State the preparation type.
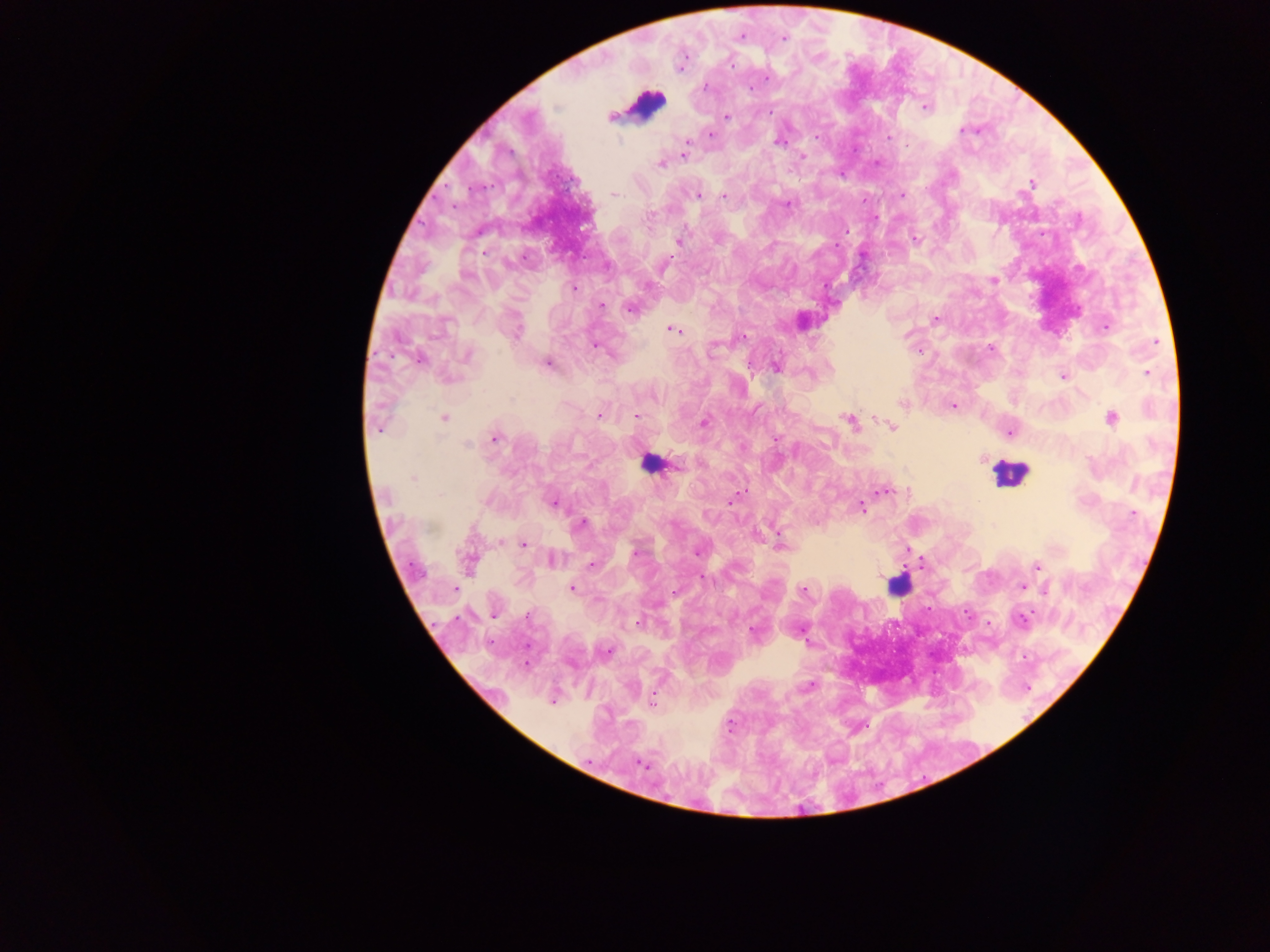

This is a thick smear.

plasmodium_parasite_locations: 'approximate centers as x y in pixels: 741 36; 783 38; 681 66; 705 87; 925 108; 727 117; 963 130; 711 134; 815 137; 889 137; 778 142; 687 143; 684 154; 802 157; 661 164; 1032 183; 614 194; 698 195; 902 195; 723 196; 788 205; 648 217; 916 238; 679 240; 993 280; 647 286; 573 288; 602 305; 631 309; 935 320; 1105 327; 674 330; 516 332; 743 337; 1155 342; 594 346; 990 348; 468 355; 418 359; 548 364; 776 367; 1147 373; 1063 376; 903 404; 954 405; 598 415; 636 416; 444 418; 1111 418; 849 420; 704 422; 892 427; 378 429; 1010 433; 495 438; 467 444; 413 478; 884 491; 737 496; 732 500; 554 503; 861 508; 1133 514; 581 524; 780 543; 523 544; 697 552; 635 553; 552 560; 468 562; 591 565; 1038 566; 703 578; 1021 587; 455 588; 573 588; 1046 589; 803 590; 493 615; 527 617; 1021 619; 638 623; 607 651; 809 687; 552 702; 652 702; 640 763'
leukocyte_locations: 'approximate centers as x y in pixels: 645 105; 650 465; 1009 472; 898 585'
field_of_view: single
country: Ghana
image_size: 1270×952 pixels
capture: mobile-phone photograph through a microscope